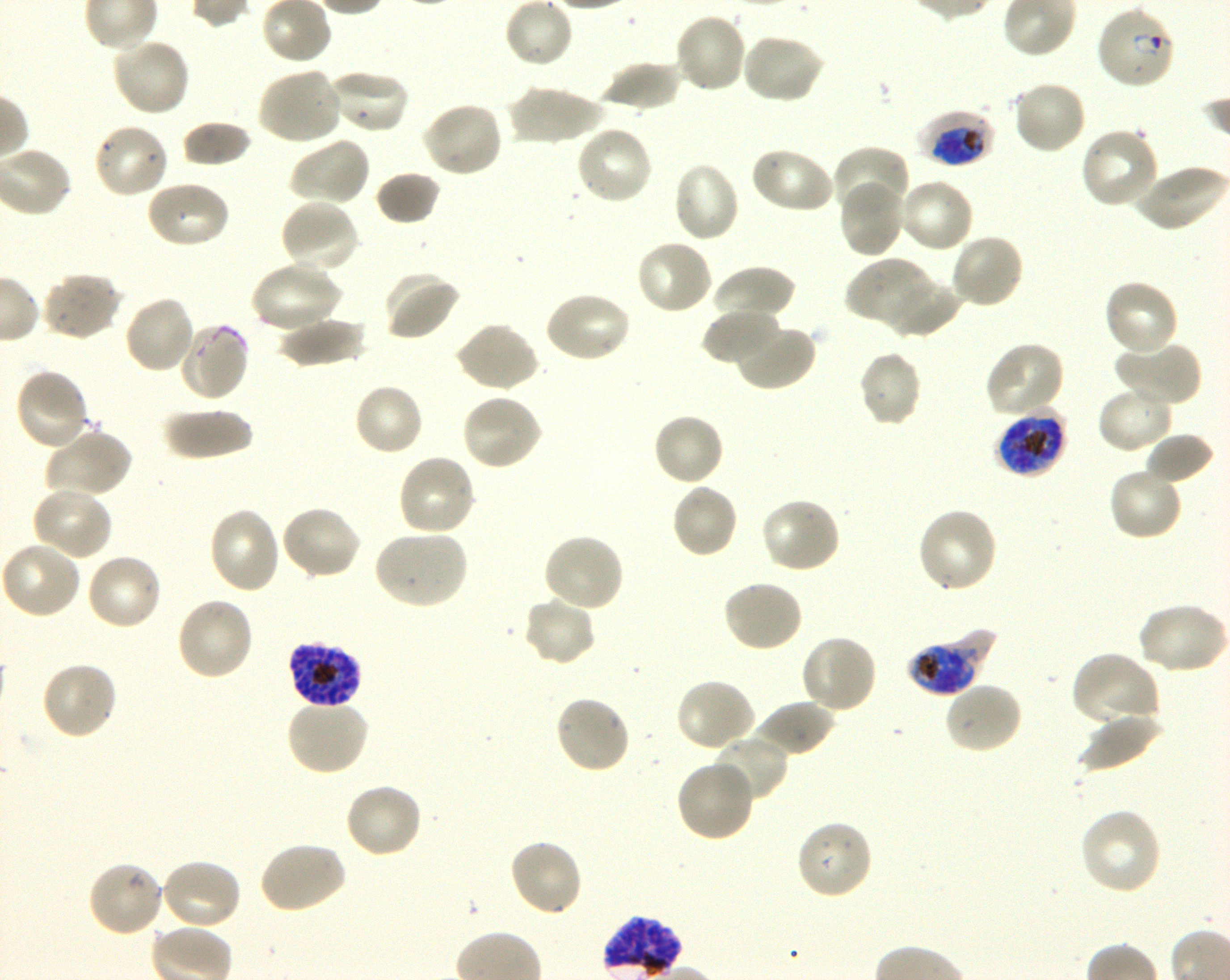
Approximate bounding boxes as (x1, y1, x2, y2) in pixels. Not every red blood cell is marked. A life-cycle stage — or a range of stages, where the recorded stages span more than one — follows each staged infected red blood cell. Locations of uninfected red blood cells: (504, 0, 573, 68), (672, 12, 748, 95), (740, 34, 826, 106), (111, 36, 191, 118), (599, 59, 682, 114), (257, 67, 343, 146), (326, 69, 410, 135), (1012, 80, 1088, 156), (505, 85, 605, 146), (421, 101, 505, 178), (181, 119, 253, 168), (92, 122, 170, 200), (573, 124, 653, 205), (1080, 127, 1161, 210), (287, 136, 371, 208), (830, 145, 909, 216), (750, 146, 835, 215), (672, 161, 741, 243), (1132, 164, 1227, 232), (375, 171, 441, 225), (897, 177, 974, 254), (144, 179, 231, 249), (838, 179, 907, 259), (279, 199, 360, 275), (949, 232, 1025, 310), (635, 239, 713, 316), (846, 257, 936, 331), (250, 261, 343, 334), (711, 265, 795, 322), (383, 270, 461, 342), (39, 272, 122, 341), (886, 278, 960, 339), (1103, 279, 1179, 357), (542, 290, 632, 364), (122, 295, 197, 375), (702, 308, 781, 366), (275, 315, 367, 368), (177, 321, 250, 401), (454, 322, 539, 393), (733, 322, 817, 391), (1115, 339, 1202, 408), (984, 340, 1066, 418), (857, 350, 922, 427), (14, 368, 91, 452), (352, 382, 425, 456), (1097, 385, 1175, 454), (461, 393, 545, 471), (161, 408, 255, 460), (652, 412, 726, 487), (43, 428, 132, 499), (1144, 431, 1214, 486), (396, 453, 476, 536), (1108, 466, 1184, 542), (670, 483, 738, 559), (32, 485, 113, 561), (760, 496, 842, 574), (280, 505, 361, 581), (208, 507, 282, 594), (915, 507, 998, 594), (372, 529, 469, 610), (541, 532, 625, 613), (1, 542, 82, 621), (84, 552, 162, 631), (721, 579, 804, 653), (174, 596, 255, 682), (522, 596, 597, 667), (1135, 602, 1228, 675), (800, 634, 878, 714), (1070, 652, 1160, 729), (39, 661, 119, 741), (675, 678, 757, 752), (943, 680, 1024, 755), (553, 695, 631, 775), (284, 698, 370, 776), (754, 700, 835, 759), (1078, 713, 1161, 773), (708, 734, 789, 803), (675, 759, 755, 843), (344, 782, 424, 859), (1078, 807, 1163, 896), (795, 819, 874, 901), (506, 838, 584, 918), (258, 841, 348, 915), (159, 858, 242, 932), (86, 859, 164, 938). Locations of infected red blood cells: (1096, 4, 1176, 90) ring; (917, 108, 994, 170) early trophozoite to early schizont; (995, 409, 1068, 478) late trophozoite to late schizont; (907, 632, 992, 695) late trophozoite to late schizont; (287, 641, 363, 709) schizont. Life-cycle stages observed: ring, schizont. One field from this slide. Giemsa stain. 100x objective under oil immersion, numerical aperture 1.30. Thin blood film. Image is 1230×980 pixels. Blood group of the donor: O+. Plasmodium falciparum strain 3D7 in shaking in-vitro culture.